Report the malaria status of this cell.
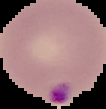

Parasitized.

Segmented cell region on a black background. From a thin blood smear. Image is 106×109 pixels.